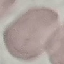 Malaria status: uninfected. Cell patch, automatically extracted from a larger field of view and resized to 64 × 64 pixels. Photographed with a smartphone camera at the microscope eyepiece. Giemsa-stained preparation. Thin blood film.